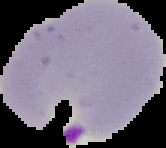

Summary:
  - Preparation: thin blood film
  - Image type: cell region segmented out of the field of view; surrounding area masked to black
  - Image size: 166×148 pixels
  - Malaria status: parasitized